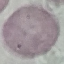

malaria status = uninfected
preparation = thin blood smear
image type = automatically extracted cell patch, resized to 64 × 64 pixels
stain = Giemsa
capture = smartphone through the microscope eyepiece